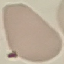
Summary:
  - Result: no malaria parasites detected
  - Capture: smartphone camera at the microscope eyepiece
  - Preparation: thin blood smear
  - Image type: automatically extracted cell patch, resized to 64 × 64 pixels
  - Stain: Giemsa